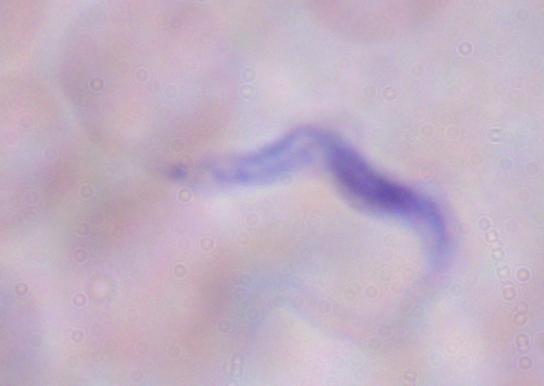

Summary:
  - Magnification: 1000x
  - Identification: trypanosome
  - Modality: micrograph